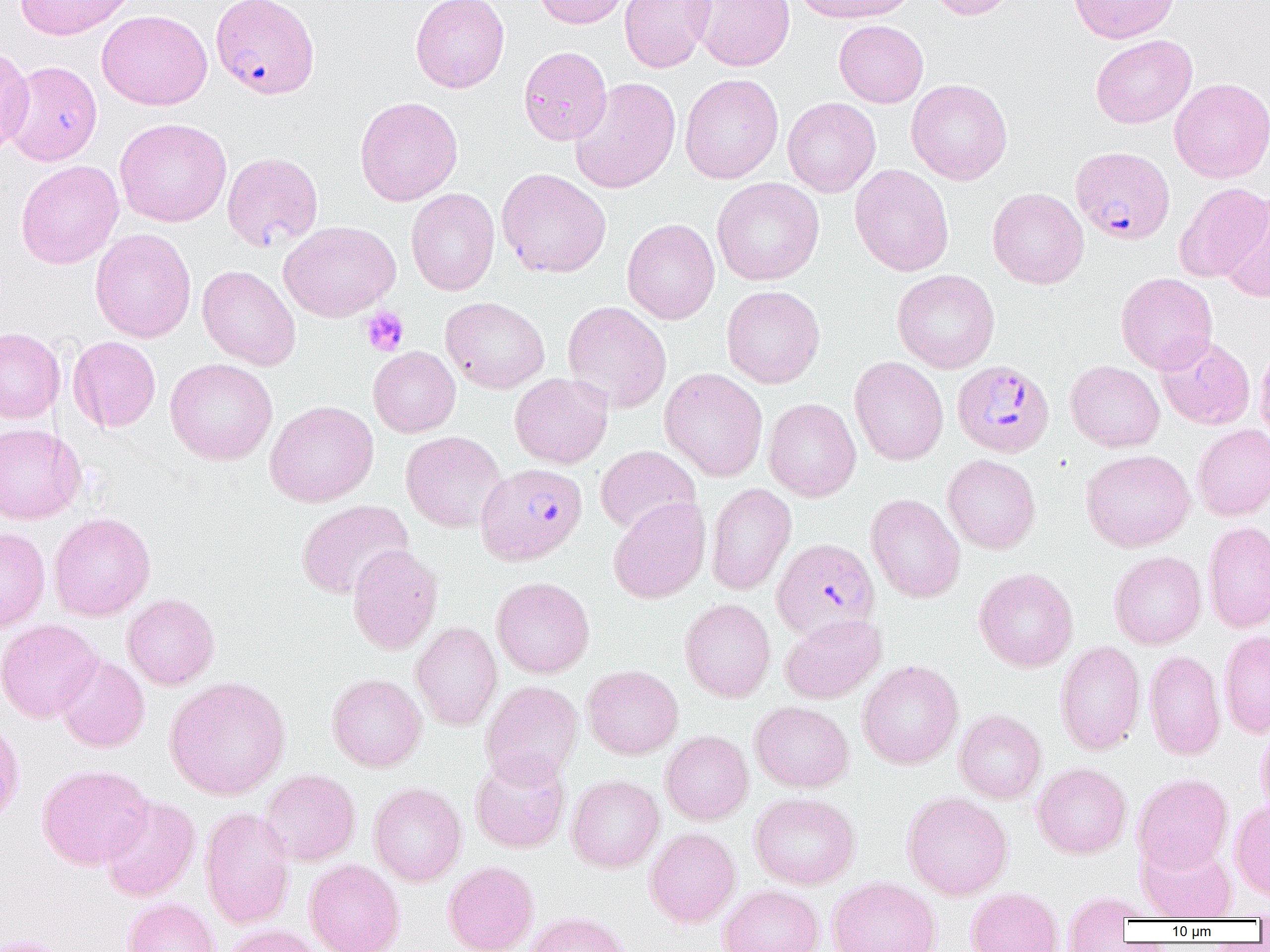

Summary:
  - Coordinate format: approximate bounding boxes as (x1,y1)-(x2,y2) corner pairs in pixels
  - Plasmodium falciparum-infected red blood cell locations: (210,0)-(319,99), (1070,146)-(1174,244), (953,363)-(1057,460), (475,462)-(587,566), (772,537)-(880,641)
  - Uninfected red blood cell locations: (14,0)-(135,40), (410,0)-(510,93), (532,0)-(630,28), (619,0)-(714,73), (689,0)-(794,71), (793,0)-(918,24), (927,0)-(1017,20), (1069,0)-(1179,43), (97,9)-(212,110), (834,20)-(928,107), (1090,35)-(1196,128), (0,46)-(33,157), (519,46)-(612,145), (4,61)-(102,165), (680,73)-(784,183), (569,77)-(680,194), (1169,78)-(1270,183), (906,79)-(1013,185), (354,96)-(463,206), (782,97)-(881,197), (115,118)-(231,227), (221,152)-(324,252), (16,160)-(123,269), (850,164)-(954,277), (497,168)-(611,278), (712,177)-(824,286), (1174,183)-(1269,282), (405,188)-(500,296), (987,188)-(1088,288), (1219,193)-(1270,303), (622,219)-(720,324), (279,220)-(400,322), (90,228)-(196,343), (197,265)-(301,370), (892,269)-(1000,373), (1116,272)-(1218,374), (721,285)-(825,388), (441,296)-(550,394), (562,301)-(671,413), (0,327)-(65,424), (1155,334)-(1255,429), (68,336)-(161,432), (1254,341)-(1270,447), (368,346)-(460,437), (849,357)-(948,466), (165,358)-(278,465), (1065,360)-(1165,451), (659,368)-(768,481), (510,373)-(613,468), (763,398)-(861,501), (265,400)-(378,507), (0,423)-(86,524), (1192,424)-(1270,521), (401,431)-(506,532), (595,445)-(701,536), (1081,449)-(1194,552), (942,454)-(1041,554), (706,483)-(797,595), (865,493)-(965,602), (608,496)-(710,604), (296,499)-(413,600), (49,512)-(155,621), (1203,521)-(1270,633), (0,527)-(51,632), (347,545)-(443,654), (1109,550)-(1206,649), (974,567)-(1078,672), (491,576)-(595,678), (122,593)-(219,689), (679,598)-(776,702), (779,613)-(886,703), (0,619)-(102,723), (410,621)-(502,731), (1219,629)-(1270,738), (1055,641)-(1146,755), (1144,649)-(1225,760), (54,654)-(150,752), (857,659)-(964,769), (582,664)-(683,759), (327,673)-(427,772), (164,676)-(291,800), (481,680)-(583,786), (751,701)-(853,792), (954,709)-(1046,804), (0,719)-(24,827), (1255,723)-(1270,819), (660,730)-(753,825), (470,751)-(570,853), (1032,762)-(1131,858), (37,764)-(153,870), (260,769)-(360,866), (1132,773)-(1233,874), (566,775)-(664,872), (368,782)-(467,886), (902,791)-(1013,900), (749,792)-(860,889), (99,796)-(200,902), (1229,799)-(1270,900), (200,806)-(296,929), (645,827)-(741,928), (1137,838)-(1238,921), (304,859)-(405,952), (443,861)-(539,952), (827,876)-(941,952), (718,885)-(824,952), (966,887)-(1063,952), (1061,892)-(1145,951), (122,897)-(221,952), (523,911)-(631,952), (223,924)-(326,952), (0,936)-(76,952)
  - Platelet locations: (360,306)-(409,356)
  - Slide-level diagnosis: Plasmodium falciparum
  - Magnification: 1000x
  - Modality: light microscopy
  - Preparation: thin blood smear
  - Image size: 1270×952 pixels
  - Field of view: single